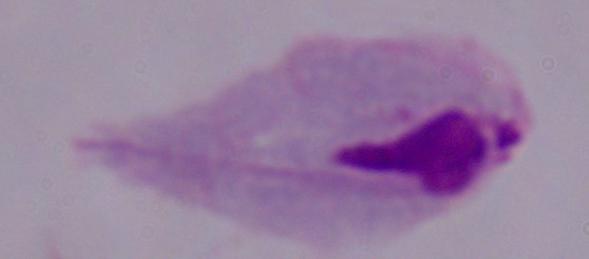

A trichomonad is seen. Captured at 1000x magnification. Micrograph.